Classify this cell by malaria status.
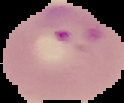

Parasitized.

Segmented cell region on a black background. Image is 124×103 pixels. From a thin blood film.